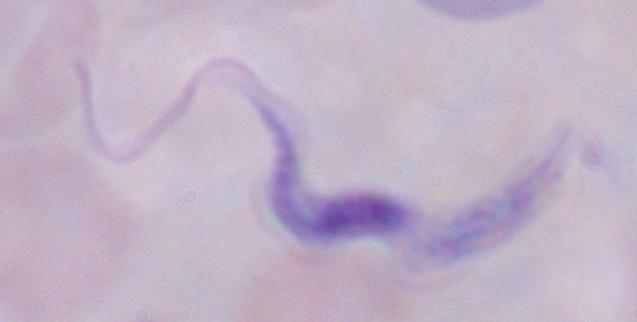

Summary:
  - Modality: photomicrograph
  - Magnification: 1000x
  - Identification: trypanosome